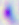 Toxoplasma gondii is shown. 400x magnification. Micrograph.